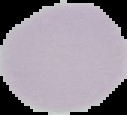

{
  "result": "negative for Plasmodium parasites",
  "image_type": "segmented cell region on a black background",
  "image_size": "127×115 pixels",
  "preparation": "thin blood film"
}